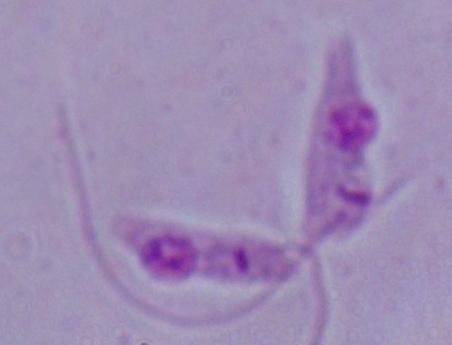

Summary:
  - Magnification: 1000x
  - Identification: Leishmania
  - Modality: micrograph